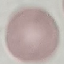

malaria status = uninfected
stain = Giemsa
capture = smartphone camera at the microscope eyepiece
image type = cell patch, automatically extracted from a larger field of view and resized to 64 × 64 pixels
preparation = thin smear